State the blood parasite species.
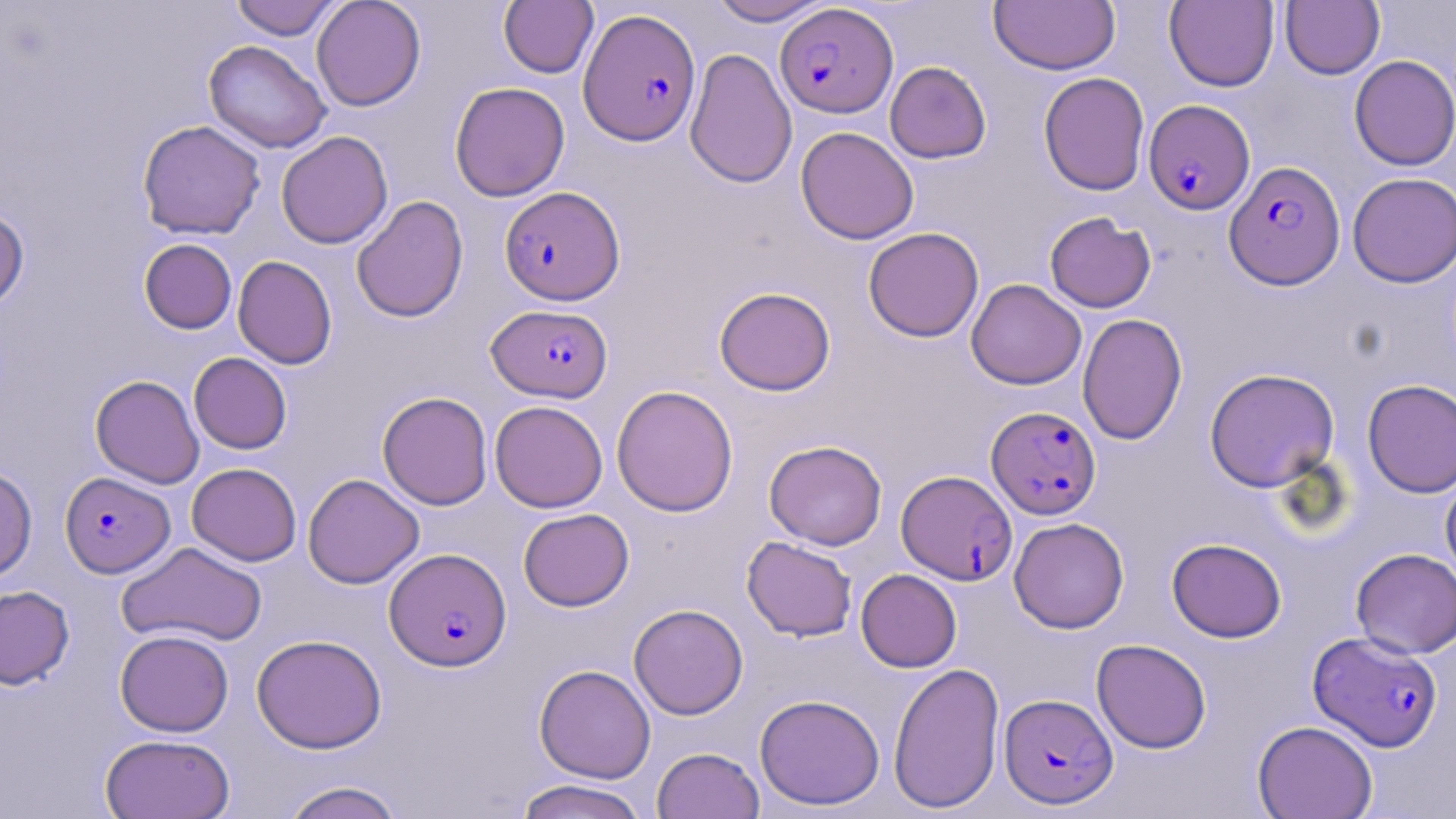

Plasmodium falciparum.

Summary:
  - Coordinate format: approximate bounding boxes as (x1,y1)-(x2,y2) corner pairs in pixels
  - Uninfected red blood cell locations: (230,0)-(341,40), (311,0)-(426,111), (498,0)-(598,78), (707,0)-(832,26), (989,1)-(1120,75), (1164,1)-(1279,92), (1280,1)-(1385,79), (203,40)-(331,153), (684,47)-(797,189), (1349,55)-(1456,171), (885,61)-(992,163), (1038,71)-(1150,195), (449,81)-(569,201), (137,120)-(265,240), (796,127)-(919,245), (276,131)-(393,249), (1347,172)-(1456,287), (351,195)-(469,323), (0,207)-(30,311), (1044,211)-(1156,313), (863,227)-(984,342), (139,239)-(237,334), (233,255)-(337,369), (966,279)-(1086,389), (714,286)-(836,395), (1078,313)-(1187,445), (189,352)-(292,454), (1204,367)-(1340,492), (90,375)-(204,488), (1362,379)-(1456,498), (611,385)-(739,517), (377,391)-(493,510), (489,400)-(608,512), (764,440)-(887,550), (187,463)-(301,565), (0,465)-(37,582), (302,473)-(424,589), (1441,474)-(1456,586), (518,508)-(634,611), (1009,517)-(1129,633), (741,536)-(857,641), (1167,537)-(1286,643), (117,541)-(267,648), (1351,548)-(1456,658), (855,569)-(961,672), (0,585)-(74,690), (628,603)-(748,719), (115,629)-(234,736), (251,633)-(387,753), (1091,638)-(1212,753), (888,661)-(1005,813), (534,664)-(656,783), (754,694)-(885,811), (1253,720)-(1378,819), (100,733)-(235,819), (652,746)-(765,819), (513,779)-(651,819), (281,780)-(406,819)
  - Plasmodium falciparum-infected red blood cell locations: (775,3)-(898,118), (579,8)-(701,146), (1144,99)-(1254,214), (1224,160)-(1345,289), (499,185)-(624,304), (487,303)-(612,403), (986,406)-(1101,520), (897,469)-(1017,584), (60,472)-(174,578), (385,548)-(511,671), (1308,631)-(1443,751), (999,693)-(1117,809)
  - Magnification: 1000x
  - Preparation: thin blood film
  - Image size: 1456×819 pixels
  - Stain: May-Grünwald-Giemsa
  - Field of view: single
  - Modality: light microscopy